Locate and identify every blood parasite.
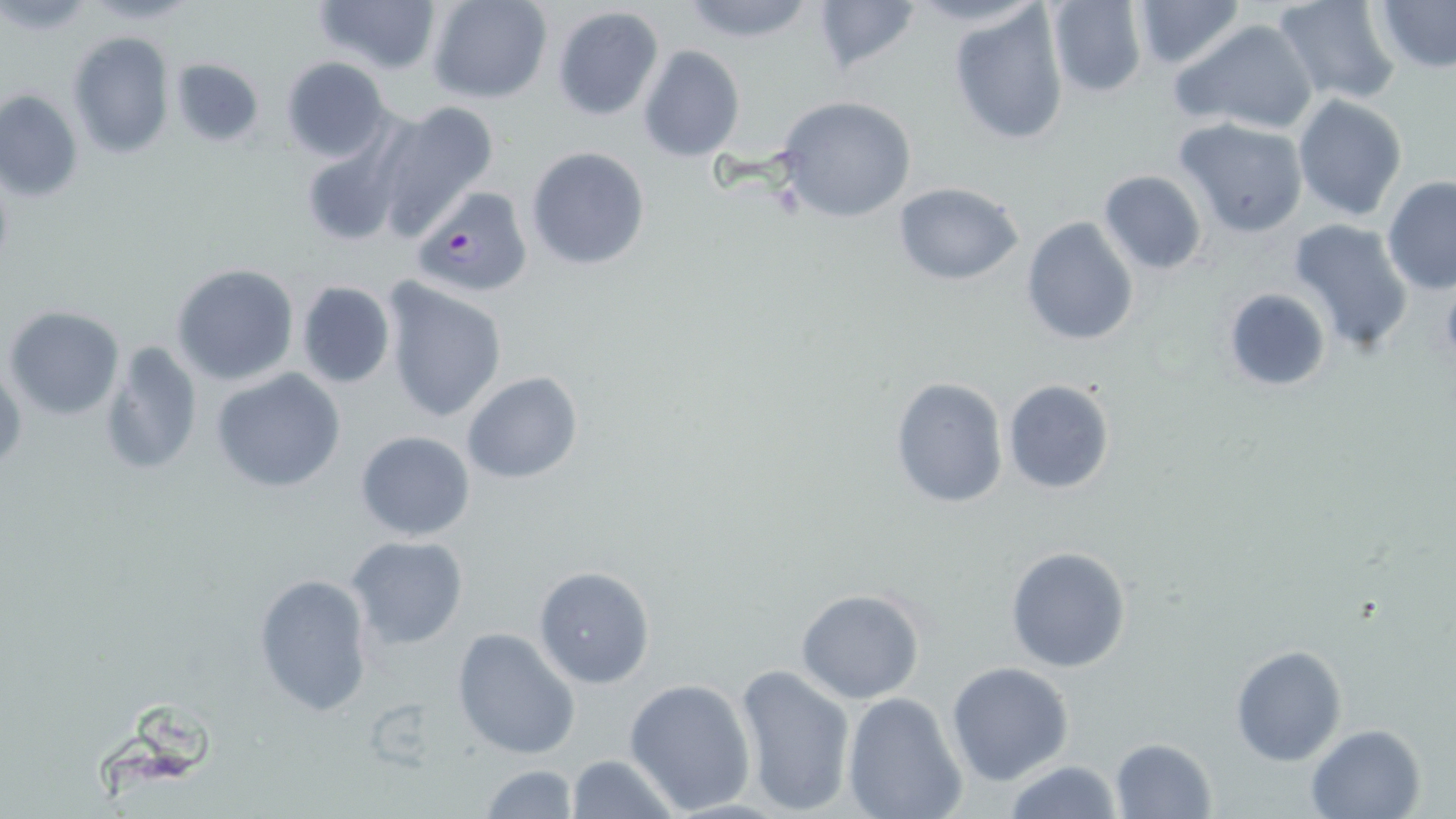

Approximate bounding boxes as (x1,y1)-(x2,y2) corner pairs in pixels.
Plasmodium falciparum-infected red blood cells: (409,188)-(538,302).
No Plasmodium ovale, Plasmodium malariae, Plasmodium vivax, Babesia divergens, or Trypanosoma brucei observed.

Summary:
  - Uninfected red blood cell locations: (311,0)-(443,77), (428,0)-(552,103), (677,0)-(820,44), (1045,0)-(1148,98), (1129,0)-(1247,70), (1272,0)-(1401,105), (1372,0)-(1456,73), (809,2)-(924,76), (948,5)-(1071,146), (552,6)-(665,123), (1171,16)-(1320,135), (68,32)-(173,158), (639,46)-(745,161), (168,55)-(267,149), (280,56)-(391,161), (1,89)-(83,202), (1291,94)-(1409,222), (774,95)-(916,223), (370,101)-(499,241), (1174,117)-(1309,236), (298,130)-(411,248), (526,146)-(651,269), (1097,169)-(1208,276), (1381,177)-(1456,294), (893,181)-(1024,285), (1020,217)-(1141,345), (1287,217)-(1415,354), (172,264)-(298,386), (382,277)-(507,423), (295,281)-(396,388), (1225,287)-(1332,392), (4,306)-(125,421), (102,340)-(203,477), (1,359)-(27,477), (211,369)-(347,494), (461,373)-(583,483), (887,376)-(1009,510), (1002,378)-(1116,495), (355,429)-(476,541), (346,537)-(469,651), (1005,544)-(1132,672), (533,565)-(655,689), (253,573)-(374,717), (794,587)-(926,704), (451,626)-(581,760), (1229,644)-(1347,766), (946,662)-(1075,785), (734,663)-(856,814), (624,678)-(756,814), (843,692)-(967,819), (1304,723)-(1426,819), (1110,737)-(1219,819), (566,754)-(679,818), (1002,760)-(1126,818), (479,762)-(576,819)
  - Slide-level diagnosis: Plasmodium falciparum
  - Magnification: 1000x
  - Preparation: thin blood smear
  - Modality: optical microscopy
  - Image size: 1456×819 pixels
  - Field of view: single
  - Stain: May-Grünwald-Giemsa